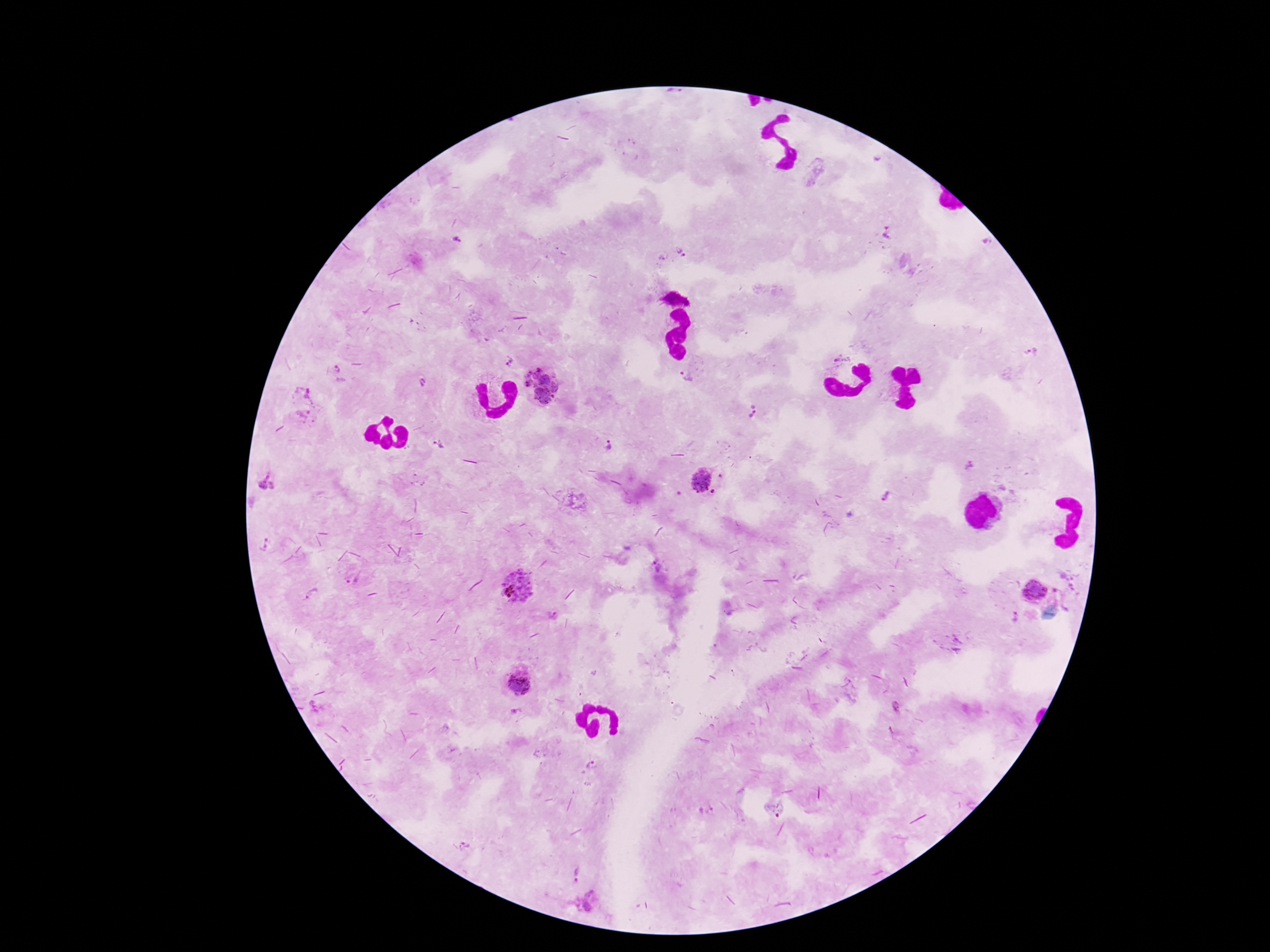
image_size: 1270×952 pixels
stain: Giemsa
field_of_view: one from this slide
patient_malaria_status: infected
capture: smartphone camera through the microscope eyepiece
preparation: thick peripheral-blood smear
plasmodium_parasite_locations: 'approximate centers as (x, y) in pixels: (888, 233), (681, 252), (663, 257), (1033, 353), (842, 359), (509, 361), (687, 377), (421, 382), (541, 384), (304, 399), (752, 411), (607, 444), (436, 445), (266, 480), (702, 480), (265, 545), (352, 578), (518, 586), (1034, 590), (312, 595), (553, 615), (517, 683), (896, 709), (515, 712), (594, 765), (706, 810), (577, 874), (589, 901)'
magnification: 100x